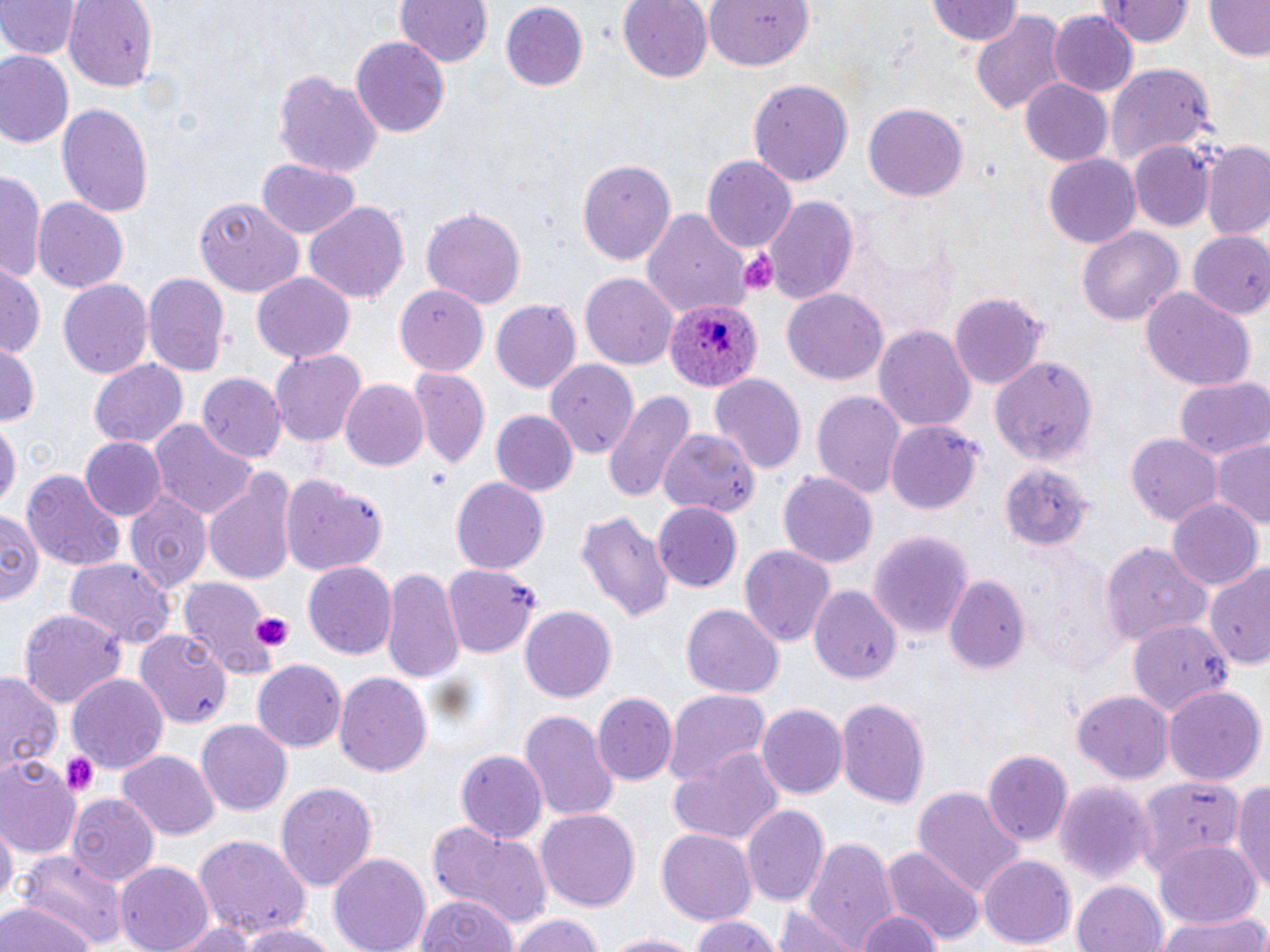
slide-level diagnosis = Plasmodium ovale
preparation = thin blood smear
magnification = 1000x
modality = light microscopy
stain = May-Grünwald-Giemsa
image size = 1270×952 pixels
field of view = one of a larger specimen
platelet locations = approximate bounding boxes as [x1, y1, x2, y2] in pixels: [736, 247, 781, 292], [426, 470, 450, 487], [250, 612, 294, 653], [60, 751, 99, 797]
Plasmodium ovale-infected red blood cell locations = approximate bounding boxes as [x1, y1, x2, y2] in pixels: [664, 298, 760, 394]
uninfected red blood cell locations = approximate bounding boxes as [x1, y1, x2, y2] in pixels: [64, 0, 156, 91], [393, 0, 493, 70], [616, 0, 714, 84], [702, 0, 812, 75], [926, 0, 1025, 48], [1105, 0, 1189, 46], [1200, 0, 1270, 63], [0, 1, 79, 62], [500, 3, 588, 91], [971, 9, 1071, 119], [1049, 10, 1136, 97], [350, 35, 451, 137], [1, 52, 74, 149], [1107, 65, 1217, 167], [271, 68, 385, 179], [749, 77, 853, 188], [1019, 79, 1113, 164], [863, 102, 968, 202], [58, 103, 152, 220], [1197, 140, 1270, 243], [1129, 142, 1214, 232], [1043, 155, 1139, 249], [704, 156, 797, 253], [578, 157, 676, 266], [257, 160, 360, 239], [1, 170, 45, 288], [764, 195, 858, 305], [33, 197, 129, 292], [193, 198, 304, 298], [304, 199, 410, 304], [46, 203, 138, 378], [421, 206, 527, 309], [641, 207, 750, 322], [1077, 225, 1183, 326], [1183, 230, 1270, 320], [0, 264, 43, 359], [142, 272, 230, 380], [251, 272, 357, 364], [580, 273, 678, 368], [57, 278, 152, 382], [393, 285, 489, 376], [781, 288, 888, 385], [1140, 288, 1255, 393], [949, 293, 1048, 387], [490, 299, 581, 395], [875, 324, 976, 435], [0, 343, 41, 427], [270, 350, 366, 447], [991, 356, 1097, 468], [88, 358, 189, 450], [545, 360, 640, 456], [408, 368, 489, 471], [198, 372, 286, 464], [709, 374, 807, 475], [1175, 377, 1270, 461], [340, 379, 430, 472], [603, 388, 692, 502], [810, 388, 907, 500], [489, 410, 578, 497], [151, 419, 257, 521], [0, 421, 18, 516], [885, 421, 983, 514], [658, 427, 758, 520], [1125, 431, 1223, 528], [78, 437, 165, 522], [1212, 441, 1270, 528], [994, 460, 1094, 556], [22, 469, 124, 573], [779, 472, 878, 570], [204, 474, 297, 588], [282, 476, 390, 575], [452, 476, 548, 573], [125, 489, 212, 595], [93, 498, 201, 637], [1167, 500, 1262, 592], [653, 502, 744, 590], [575, 509, 673, 624], [0, 510, 45, 610], [867, 528, 976, 639], [738, 543, 836, 648], [1102, 543, 1213, 647], [63, 557, 177, 649], [304, 561, 400, 657], [1203, 562, 1270, 670], [443, 565, 542, 658], [381, 566, 466, 688], [176, 576, 277, 678], [946, 576, 1031, 675], [810, 585, 900, 685], [681, 604, 783, 697], [520, 606, 616, 703], [19, 609, 124, 712], [1128, 618, 1234, 721], [136, 630, 233, 729], [252, 659, 345, 753], [0, 670, 62, 780], [335, 671, 433, 778], [67, 672, 170, 776], [1163, 684, 1266, 786], [666, 688, 773, 786], [1074, 690, 1175, 783], [593, 693, 678, 786], [835, 697, 929, 809], [756, 701, 848, 799], [519, 709, 618, 819], [198, 721, 292, 814], [667, 748, 786, 850], [982, 749, 1072, 845], [455, 750, 548, 844], [119, 751, 218, 839], [0, 757, 82, 858], [1133, 773, 1248, 879], [1232, 775, 1270, 898], [275, 779, 377, 895], [1053, 780, 1154, 883], [912, 787, 1024, 900], [68, 794, 160, 886], [740, 803, 830, 906], [537, 810, 640, 911], [0, 820, 16, 912], [426, 820, 555, 928], [657, 828, 759, 924], [803, 833, 897, 950], [192, 836, 309, 941], [1154, 841, 1261, 930], [882, 844, 984, 948], [17, 851, 126, 951], [327, 851, 432, 952], [979, 855, 1073, 949], [116, 862, 215, 952], [1071, 879, 1170, 952], [415, 894, 518, 952], [0, 901, 98, 952], [773, 909, 860, 952], [1156, 909, 1266, 952], [852, 911, 947, 952], [507, 912, 605, 952], [689, 917, 783, 952], [164, 918, 260, 952], [236, 924, 340, 952], [602, 931, 704, 952]